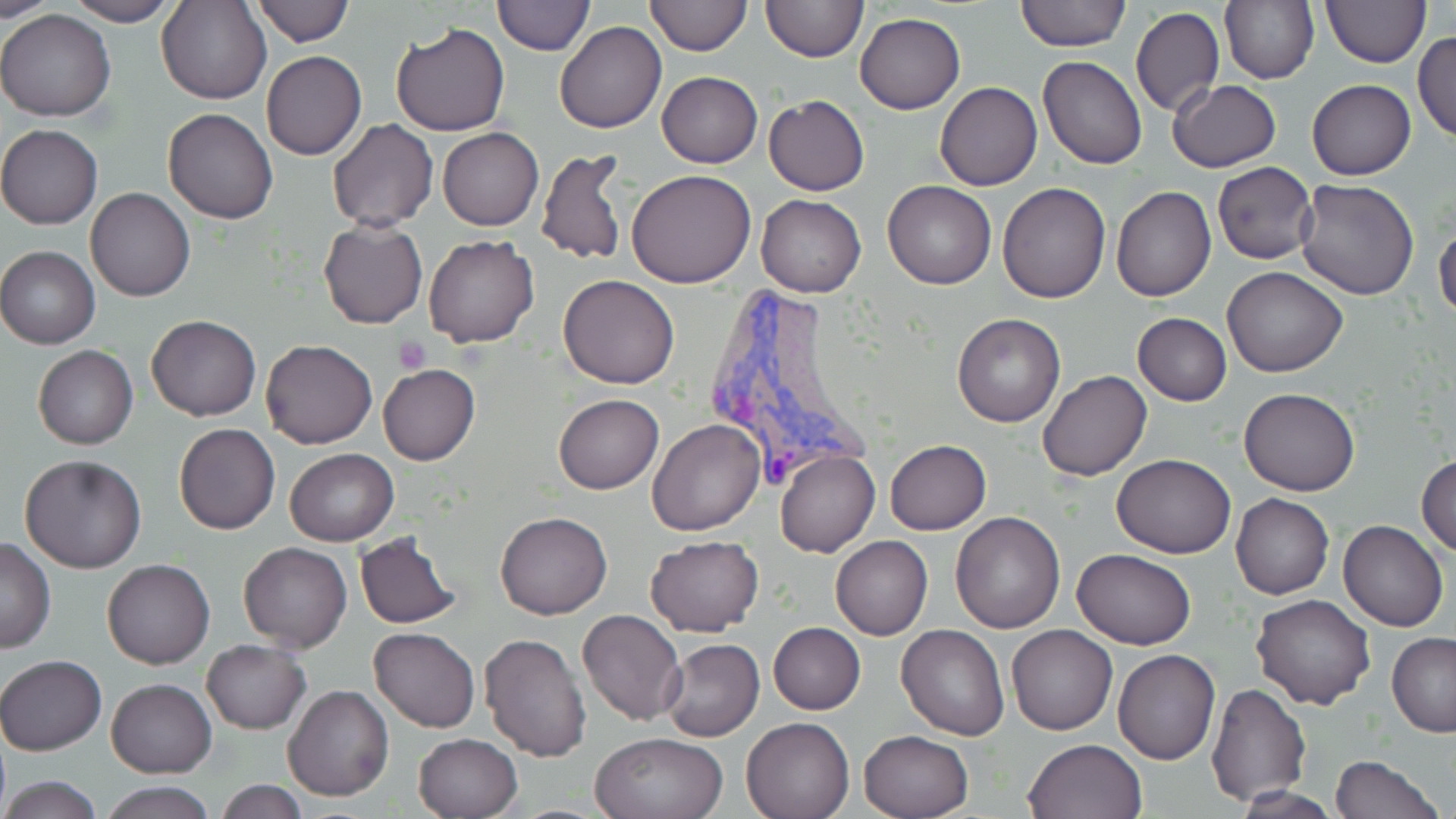

slide-level diagnosis = Plasmodium vivax
modality = light microscopy
stain = May-Grünwald-Giemsa
Plasmodium vivax-infected red blood cell locations = approximate bounding boxes as [x1, y1, x2, y2] in pixels: [708, 283, 876, 488]
image size = 1456×819 pixels
uninfected red blood cell locations = approximate bounding boxes as [x1, y1, x2, y2] in pixels: [0, 0, 57, 21], [158, 0, 270, 105], [250, 0, 354, 46], [494, 0, 594, 57], [643, 0, 750, 56], [760, 0, 867, 64], [1014, 0, 1130, 51], [1221, 0, 1318, 85], [1321, 0, 1431, 67], [64, 1, 178, 26], [1131, 5, 1224, 116], [0, 9, 118, 123], [856, 12, 965, 113], [555, 21, 667, 134], [389, 22, 511, 135], [1413, 31, 1456, 144], [261, 50, 366, 160], [1039, 57, 1148, 169], [657, 70, 763, 167], [1168, 79, 1281, 172], [1307, 79, 1415, 180], [934, 82, 1042, 191], [764, 95, 869, 196], [163, 108, 277, 224], [328, 119, 438, 232], [0, 124, 102, 229], [438, 127, 543, 230], [537, 146, 631, 269], [1212, 162, 1320, 264], [626, 169, 756, 287], [883, 179, 996, 289], [1294, 179, 1420, 300], [997, 182, 1109, 302], [86, 186, 196, 302], [1112, 186, 1216, 302], [759, 195, 865, 298], [318, 218, 428, 330], [1434, 221, 1456, 325], [424, 234, 539, 348], [0, 247, 100, 348], [1222, 267, 1347, 377], [559, 275, 679, 389], [1132, 312, 1232, 406], [952, 313, 1065, 428], [146, 315, 262, 421], [261, 339, 378, 449], [33, 346, 137, 448], [378, 364, 481, 466], [1039, 370, 1151, 482], [1239, 387, 1359, 495], [552, 394, 663, 494], [647, 420, 764, 536], [174, 423, 281, 535], [885, 439, 992, 534], [285, 448, 399, 545], [775, 449, 881, 558], [19, 454, 147, 573], [1416, 454, 1456, 557], [1113, 455, 1236, 558], [1231, 494, 1333, 600], [495, 511, 612, 620], [950, 511, 1066, 632], [1338, 520, 1448, 632], [354, 533, 461, 629], [644, 535, 764, 638], [830, 535, 933, 641], [0, 539, 56, 653], [238, 541, 352, 652], [1071, 547, 1198, 650], [102, 559, 214, 668], [1252, 594, 1376, 711], [577, 610, 687, 728], [768, 622, 865, 714], [897, 624, 1008, 740], [1006, 624, 1116, 735], [369, 626, 479, 733], [480, 631, 593, 760], [1387, 633, 1456, 737], [660, 638, 764, 742], [201, 640, 311, 734], [1113, 648, 1221, 764], [1, 654, 106, 755], [106, 679, 216, 778], [1206, 682, 1312, 804], [284, 685, 393, 802], [740, 717, 853, 819], [858, 730, 974, 819], [590, 731, 728, 819], [412, 733, 524, 819], [1023, 739, 1148, 819], [1331, 754, 1442, 818], [0, 775, 104, 817], [212, 779, 310, 818], [97, 780, 219, 819]
preparation = thin blood smear
magnification = 1000x
field of view = single
platelet locations = approximate bounding boxes as [x1, y1, x2, y2] in pixels: [395, 337, 430, 374]